Locate every Plasmodium ovale-infected red blood cell.
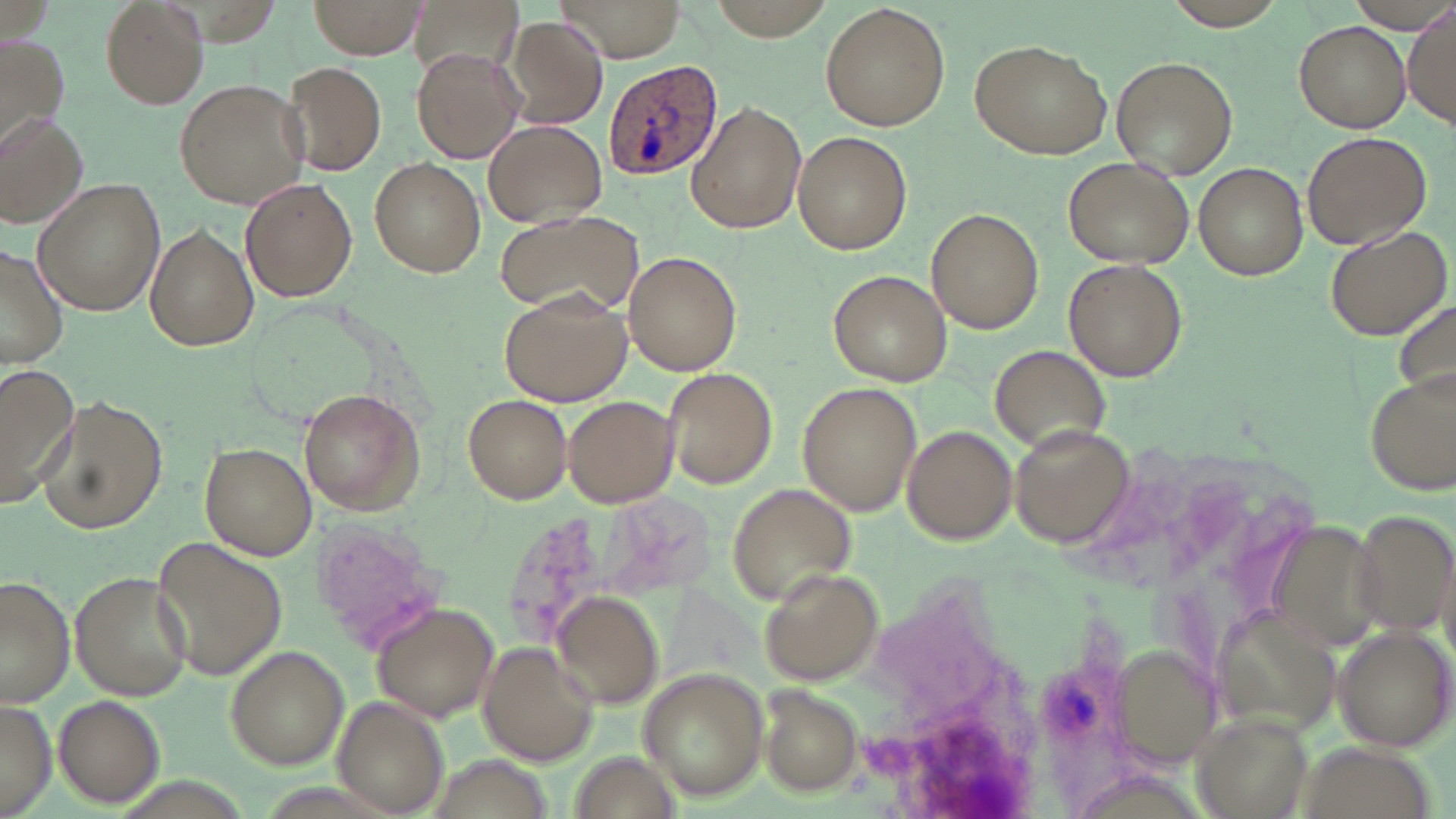
Approximate bounding boxes as (x1,y1)-(x2,y2) corner pairs in pixels.
Plasmodium ovale-infected red blood cells: (602,59)-(724,179).

slide-level diagnosis = Plasmodium ovale
uninfected red blood cell locations = approximate bounding boxes as (x1,y1)-(x2,y2) corner pairs in pixels: (98,0)-(209,110), (310,0)-(428,59), (557,0)-(686,62), (702,0)-(843,38), (1152,1)-(1299,30), (410,2)-(523,87), (820,4)-(951,133), (1405,5)-(1455,129), (501,15)-(610,130), (1294,19)-(1410,132), (0,36)-(69,149), (971,38)-(1111,159), (411,50)-(522,164), (1110,56)-(1238,178), (282,63)-(387,177), (174,78)-(308,210), (688,101)-(806,236), (0,113)-(88,230), (484,119)-(607,227), (792,131)-(911,253), (1303,132)-(1432,249), (1064,156)-(1192,270), (370,157)-(485,277), (1194,162)-(1309,280), (240,177)-(358,303), (33,180)-(163,317), (927,208)-(1045,333), (494,211)-(641,320), (146,224)-(260,353), (1323,225)-(1452,338), (0,248)-(70,371), (624,251)-(742,375), (1064,259)-(1183,381), (828,270)-(951,386), (500,286)-(633,405), (1392,302)-(1456,397), (990,344)-(1107,452), (0,364)-(82,504), (661,366)-(776,489), (1365,367)-(1455,496), (797,382)-(921,514), (298,388)-(426,515), (461,394)-(572,503), (37,396)-(167,534), (564,396)-(680,507), (902,425)-(1017,546), (1013,427)-(1130,547), (201,443)-(316,561), (729,483)-(858,605), (1344,510)-(1454,636), (494,511)-(620,650), (1259,517)-(1386,653), (312,519)-(444,652), (151,535)-(288,682), (760,567)-(885,688), (70,572)-(193,700), (0,575)-(76,705), (551,593)-(663,705), (370,600)-(499,725), (1207,603)-(1343,732), (1332,626)-(1455,752), (476,643)-(597,766), (225,645)-(349,769), (1116,645)-(1226,766), (637,667)-(769,799), (761,688)-(863,796), (52,693)-(166,808), (334,695)-(451,817), (0,697)-(56,818), (1191,713)-(1314,818), (1289,737)-(1434,818), (565,750)-(683,819)
modality = light microscopy
image size = 1456×819 pixels
magnification = 1000x
field of view = single
preparation = thin blood smear
stain = May-Grünwald-Giemsa